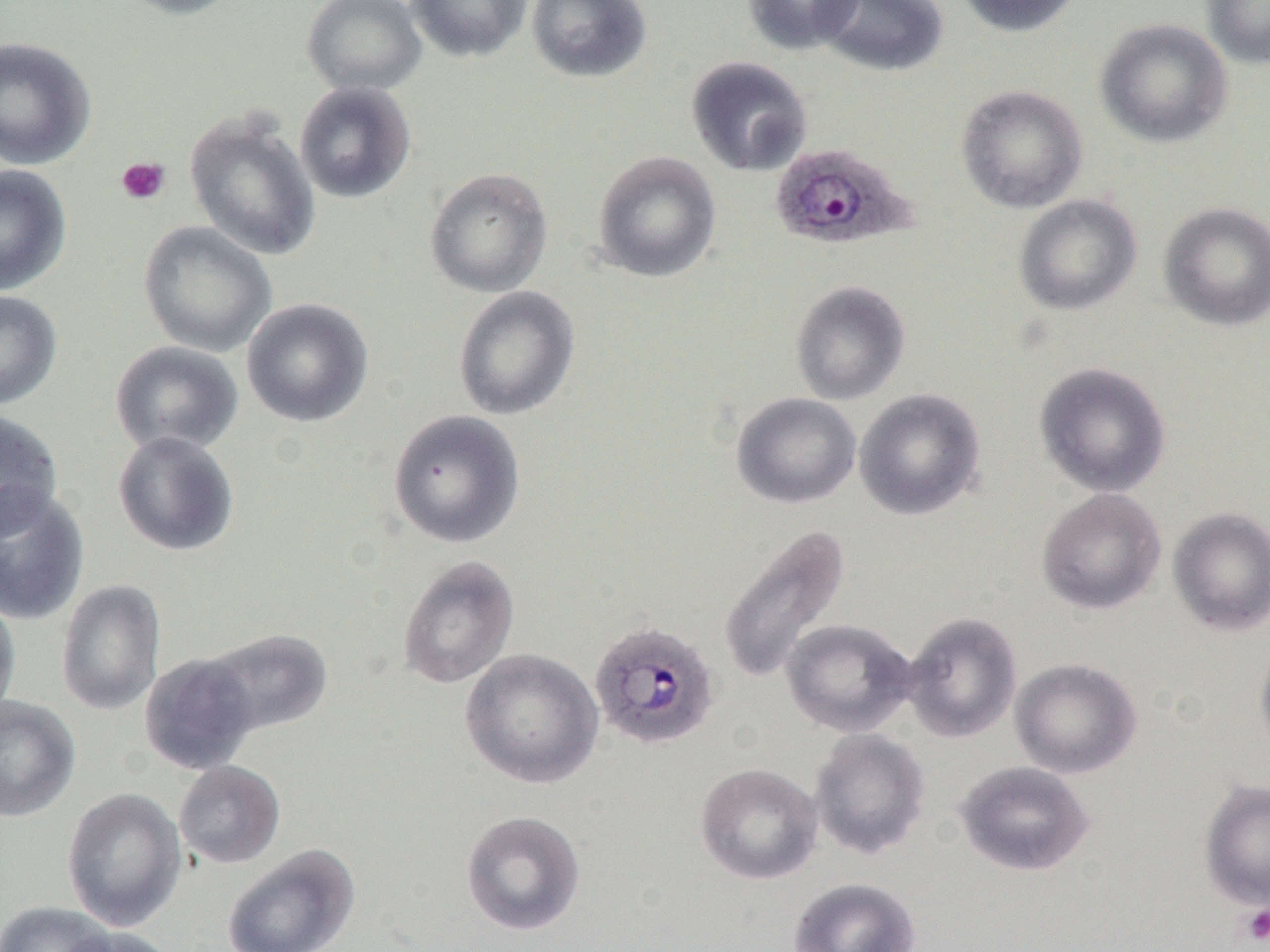
plasmodium_ovale_infected_red_blood_cell_locations: 'approximate bounding boxes as (x1, y1, x2, y2) in pixels: (770, 142, 918, 250), (588, 620, 721, 750)'
slide_level_diagnosis: Plasmodium ovale
image_size: 1270×952 pixels
platelet_locations: 'approximate bounding boxes as (x1, y1, x2, y2) in pixels: (115, 156, 171, 206), (1240, 904, 1270, 946)'
field_of_view: single
modality: light microscopy
uninfected_red_blood_cell_locations: 'approximate bounding boxes as (x1, y1, x2, y2) in pixels: (112, 0, 245, 19), (301, 0, 428, 96), (406, 0, 533, 63), (526, 0, 652, 83), (742, 0, 864, 54), (817, 0, 948, 77), (954, 0, 1083, 37), (1202, 0, 1270, 69), (1095, 17, 1234, 148), (0, 37, 96, 170), (686, 56, 813, 177), (294, 81, 416, 204), (955, 84, 1088, 214), (184, 110, 321, 261), (591, 150, 722, 283), (0, 165, 72, 296), (424, 167, 553, 298), (1013, 194, 1143, 316), (1158, 201, 1270, 331), (138, 221, 277, 357), (789, 280, 910, 405), (453, 285, 581, 420), (0, 291, 62, 410), (241, 297, 374, 428), (109, 340, 244, 457), (1033, 361, 1171, 497), (854, 388, 986, 520), (731, 392, 861, 509), (0, 408, 64, 537), (386, 409, 525, 548), (112, 430, 240, 557), (0, 484, 90, 626), (1036, 488, 1166, 615), (1167, 507, 1270, 636), (717, 523, 851, 686), (397, 555, 520, 690), (55, 579, 166, 716), (0, 593, 21, 720), (901, 611, 1022, 743), (781, 618, 917, 736), (201, 627, 334, 736), (1254, 638, 1270, 759), (460, 648, 604, 789), (139, 653, 260, 775), (1009, 657, 1142, 778), (0, 695, 80, 822), (809, 728, 930, 859), (954, 760, 1095, 876), (174, 761, 285, 868), (695, 762, 823, 885), (1199, 779, 1270, 909), (61, 787, 186, 931), (461, 809, 586, 936), (222, 844, 360, 952), (787, 877, 920, 952), (0, 901, 115, 952), (55, 926, 177, 952)'
magnification: 1000x
preparation: thin blood smear